Assess for parasitized red blood cells.
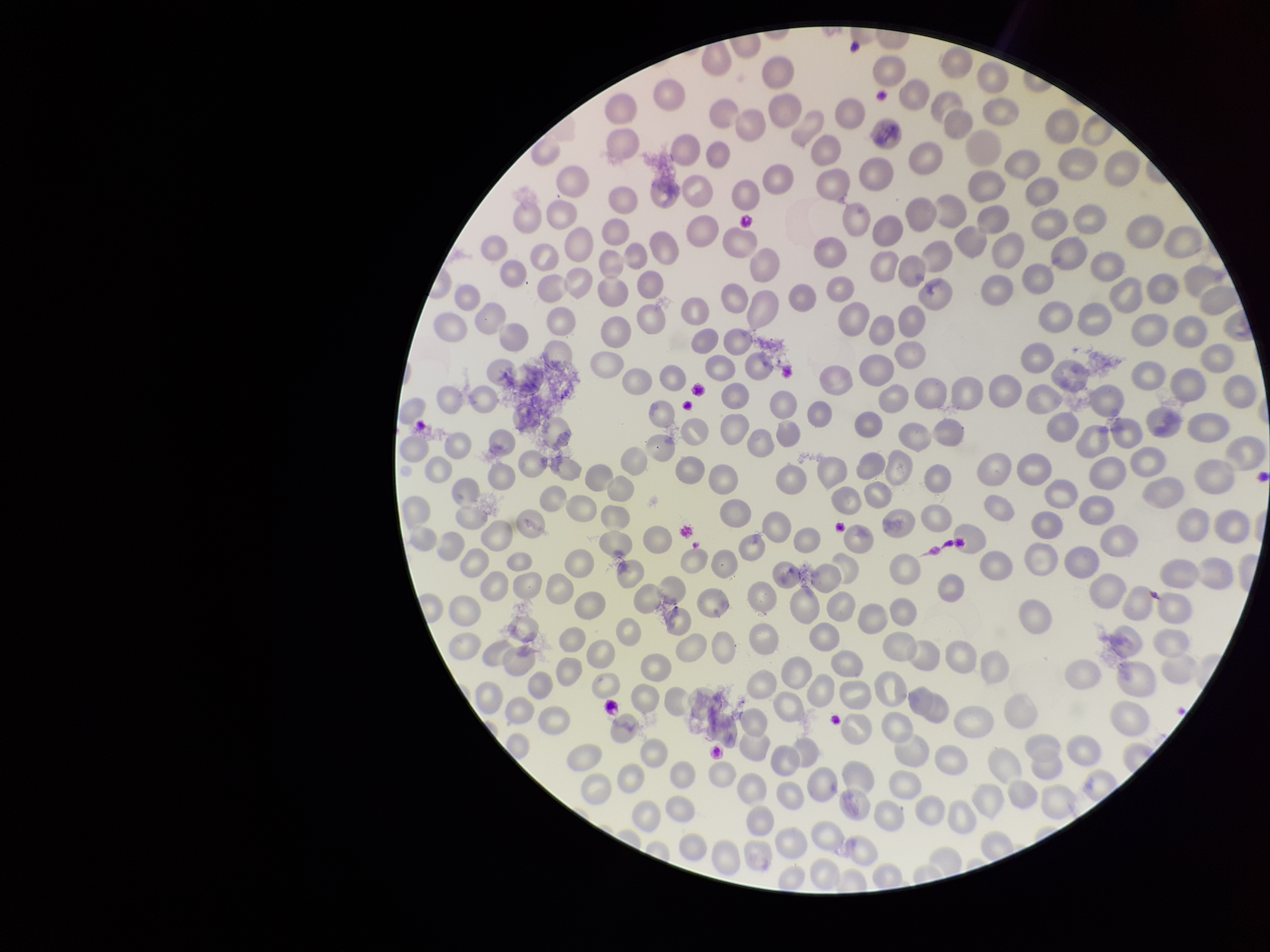

None seen.

Preparation: thin blood smear. One field from this slide. Parasitized red blood cell count: 0. Photographed through the microscope eyepiece with a smartphone camera. Red blood cell count: 266. Giemsa stain. Patient malaria status: negative. Image is 1270×952 pixels.